State which parasite is depicted.
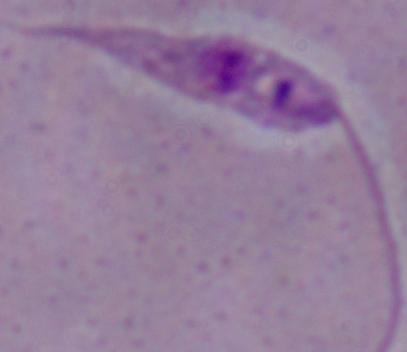

Leishmania.

1000x magnification. Photomicrograph.